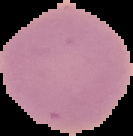

preparation = thin blood film
image size = 133×136 pixels
image type = segmented cell region with the area outside set to black
malaria status = uninfected